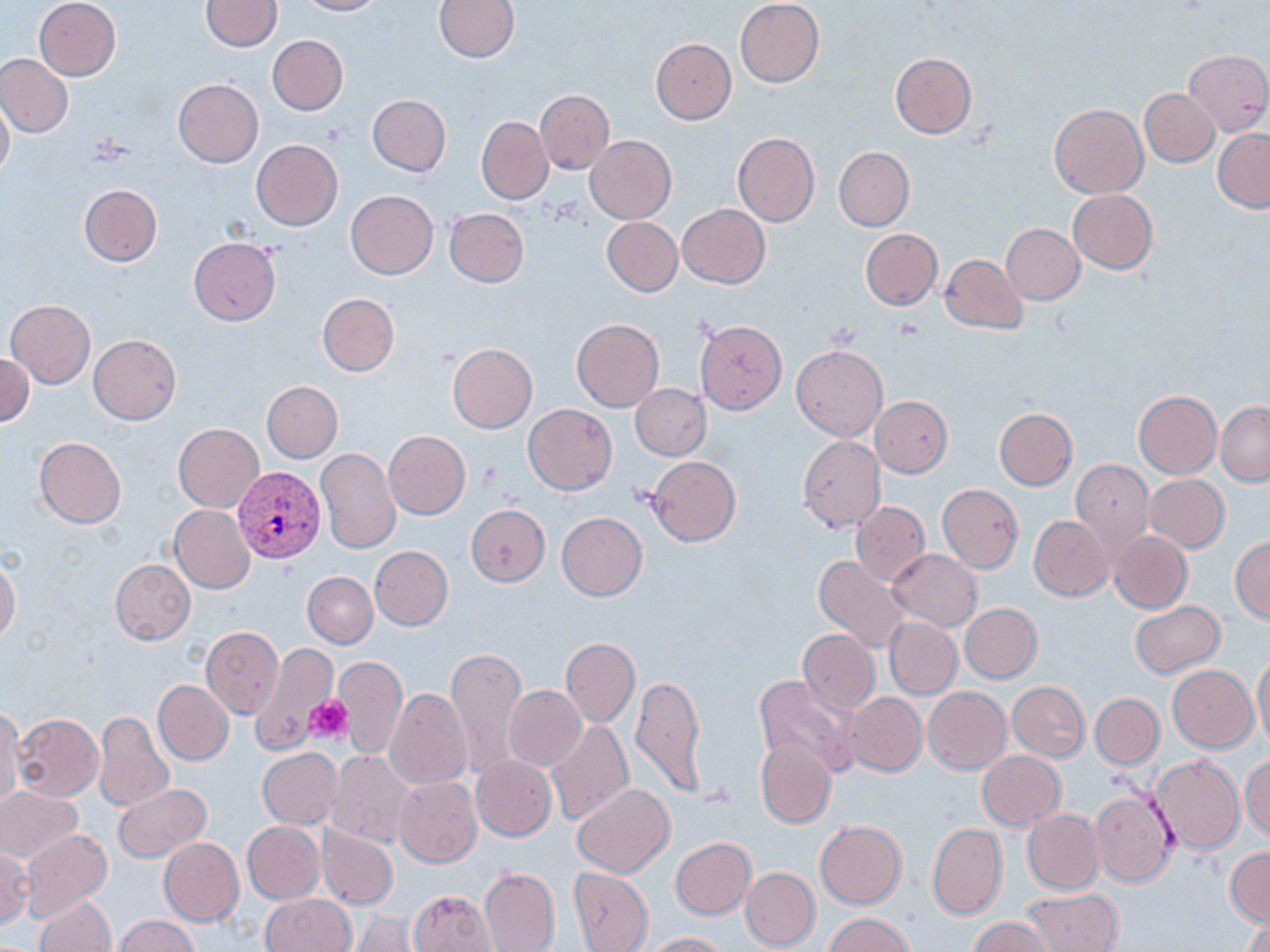

Summary:
  - Coordinate format: approximate bounding boxes as [x1, y1, x2, y2] in pixels
  - Platelet locations: [306, 697, 352, 745], [703, 783, 736, 809]
  - Uninfected red blood cell locations: [33, 0, 121, 81], [200, 0, 282, 51], [295, 0, 385, 16], [433, 0, 521, 63], [735, 1, 825, 87], [266, 36, 348, 115], [650, 37, 736, 124], [1182, 49, 1270, 135], [891, 53, 976, 137], [0, 54, 73, 138], [172, 79, 263, 168], [1140, 88, 1219, 165], [535, 90, 615, 174], [367, 94, 451, 177], [0, 95, 13, 182], [1049, 104, 1148, 199], [476, 116, 553, 204], [1213, 128, 1270, 212], [732, 132, 818, 227], [585, 135, 675, 223], [251, 139, 342, 230], [834, 147, 914, 231], [79, 184, 162, 266], [345, 190, 438, 279], [1068, 190, 1158, 274], [678, 203, 770, 289], [444, 208, 529, 286], [601, 217, 682, 296], [1001, 224, 1083, 304], [860, 229, 942, 310], [188, 238, 280, 325], [940, 253, 1028, 333], [318, 293, 399, 377], [5, 300, 95, 389], [571, 318, 664, 411], [695, 321, 786, 413], [88, 335, 180, 424], [448, 343, 537, 433], [791, 344, 887, 441], [0, 353, 34, 428], [262, 382, 342, 462], [630, 384, 710, 459], [1133, 391, 1221, 478], [870, 396, 953, 477], [522, 402, 617, 495], [1215, 402, 1270, 485], [994, 408, 1077, 489], [173, 423, 263, 512], [383, 432, 470, 518], [798, 436, 886, 531], [33, 437, 127, 528], [316, 448, 400, 554], [646, 456, 740, 546], [1071, 460, 1154, 558], [1144, 474, 1229, 552], [937, 485, 1022, 572], [850, 500, 930, 587], [170, 504, 255, 594], [466, 504, 550, 585], [557, 512, 646, 600], [1029, 515, 1113, 601], [1108, 530, 1192, 614], [1230, 535, 1270, 624], [370, 546, 452, 630], [888, 549, 982, 631], [813, 554, 910, 652], [0, 557, 20, 644], [110, 558, 195, 644], [303, 571, 378, 648], [1130, 600, 1225, 678], [960, 603, 1042, 683], [883, 616, 962, 698], [200, 625, 283, 720], [797, 629, 879, 713], [560, 638, 638, 727], [249, 642, 336, 754], [446, 647, 526, 780], [1253, 651, 1270, 749], [335, 655, 407, 759], [1168, 665, 1258, 752], [337, 667, 464, 776], [631, 673, 707, 799], [754, 676, 858, 777], [153, 679, 233, 765], [1008, 681, 1090, 761], [503, 686, 586, 772], [384, 687, 473, 789], [923, 687, 1011, 773], [843, 693, 927, 776], [1091, 693, 1164, 767], [0, 705, 23, 806], [94, 710, 174, 811], [12, 713, 104, 801], [546, 719, 634, 826], [755, 737, 837, 828], [257, 748, 342, 829], [326, 750, 414, 847], [977, 751, 1064, 829], [470, 754, 556, 841], [1151, 755, 1244, 854], [1240, 755, 1270, 843], [393, 776, 482, 868], [572, 783, 674, 877], [113, 784, 211, 863], [0, 787, 81, 862], [1091, 788, 1178, 886], [1022, 810, 1103, 894], [815, 820, 907, 908], [242, 821, 324, 904], [927, 823, 1007, 920], [316, 824, 397, 910], [21, 829, 111, 922], [158, 838, 243, 925], [670, 838, 756, 920], [1, 848, 32, 928], [1226, 848, 1269, 927], [480, 866, 559, 952], [569, 866, 653, 951], [741, 867, 820, 951], [1021, 889, 1124, 952], [409, 890, 496, 952], [261, 894, 355, 952], [34, 896, 114, 952], [350, 913, 423, 951], [824, 913, 913, 952], [116, 916, 198, 952], [968, 916, 1058, 951], [1241, 916, 1270, 952], [645, 932, 728, 952]
  - Plasmodium vivax-infected red blood cell locations: [233, 466, 327, 563]
  - Slide-level diagnosis: Plasmodium vivax
  - Field of view: single
  - Preparation: thin blood film
  - Image size: 1270×952 pixels
  - Magnification: 1000x
  - Modality: optical microscopy
  - Stain: May-Grünwald-Giemsa